Identify the parasite.
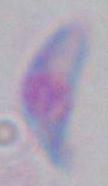
Toxoplasma gondii.

magnification: 1000x
modality: micrograph